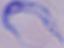
magnification = 1000x
modality = photomicrograph
identification = trypanosome